Classify this cell by malaria status.
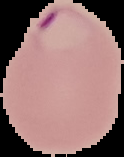

It is parasitized.

Summary:
  - Image size: 124×157 pixels
  - Image type: segmented cell region with the area outside set to black
  - Preparation: thin blood film